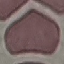
Malaria status: uninfected. Cell patch, automatically extracted from a larger field of view and resized to 64 × 64 pixels. Photographed with a smartphone camera at the microscope eyepiece. Giemsa-stained preparation. Thin smear of blood.